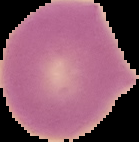

Summary:
  - Image type: segmented cell region with the area outside set to black
  - Preparation: thin blood smear
  - Malaria status: uninfected
  - Image size: 139×142 pixels